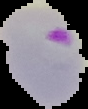
Summary:
  - Result: malaria parasites detected
  - Image size: 88×109 pixels
  - Preparation: thin blood smear
  - Image type: segmented cell region on a black background